Assess this cell for malaria.
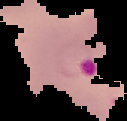

Parasitized.

image type = cell region segmented out of the field of view; surrounding area masked to black
preparation = thin blood film
image size = 127×121 pixels